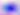

Photomicrograph. Captured at 400x magnification. Toxoplasma gondii is shown.